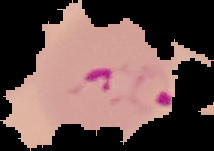
image type = segmented cell region on a black background
image size = 214×151 pixels
preparation = thin blood smear
result = malaria parasites detected